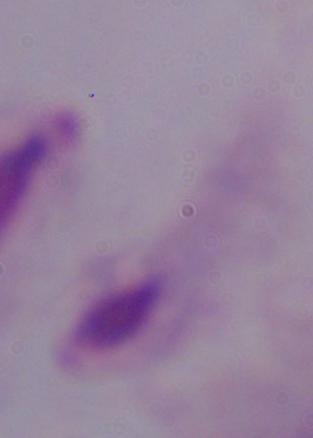
identification = trichomonad
magnification = 1000x
modality = micrograph